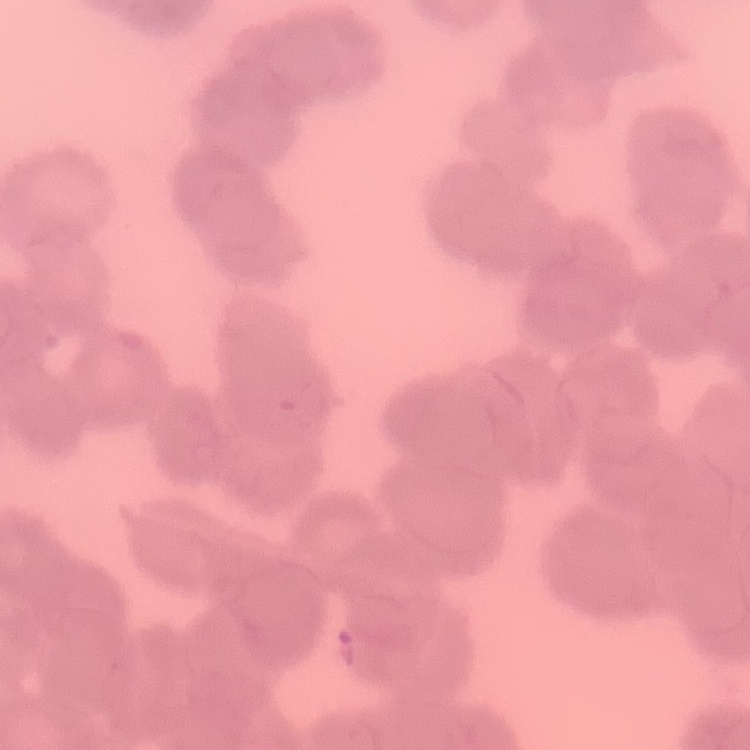
erythrocyte morphology = rouleaux formation
stain = Field's or Giemsa
image type = one tile cut from a larger photomicrograph
preparation = thin blood film